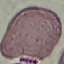

Summary:
  - Malaria status: uninfected
  - Stain: Giemsa
  - Preparation: thin smear
  - Image type: cell patch, automatically extracted from a larger field of view and resized to 64 × 64 pixels
  - Capture: smartphone camera at the microscope eyepiece